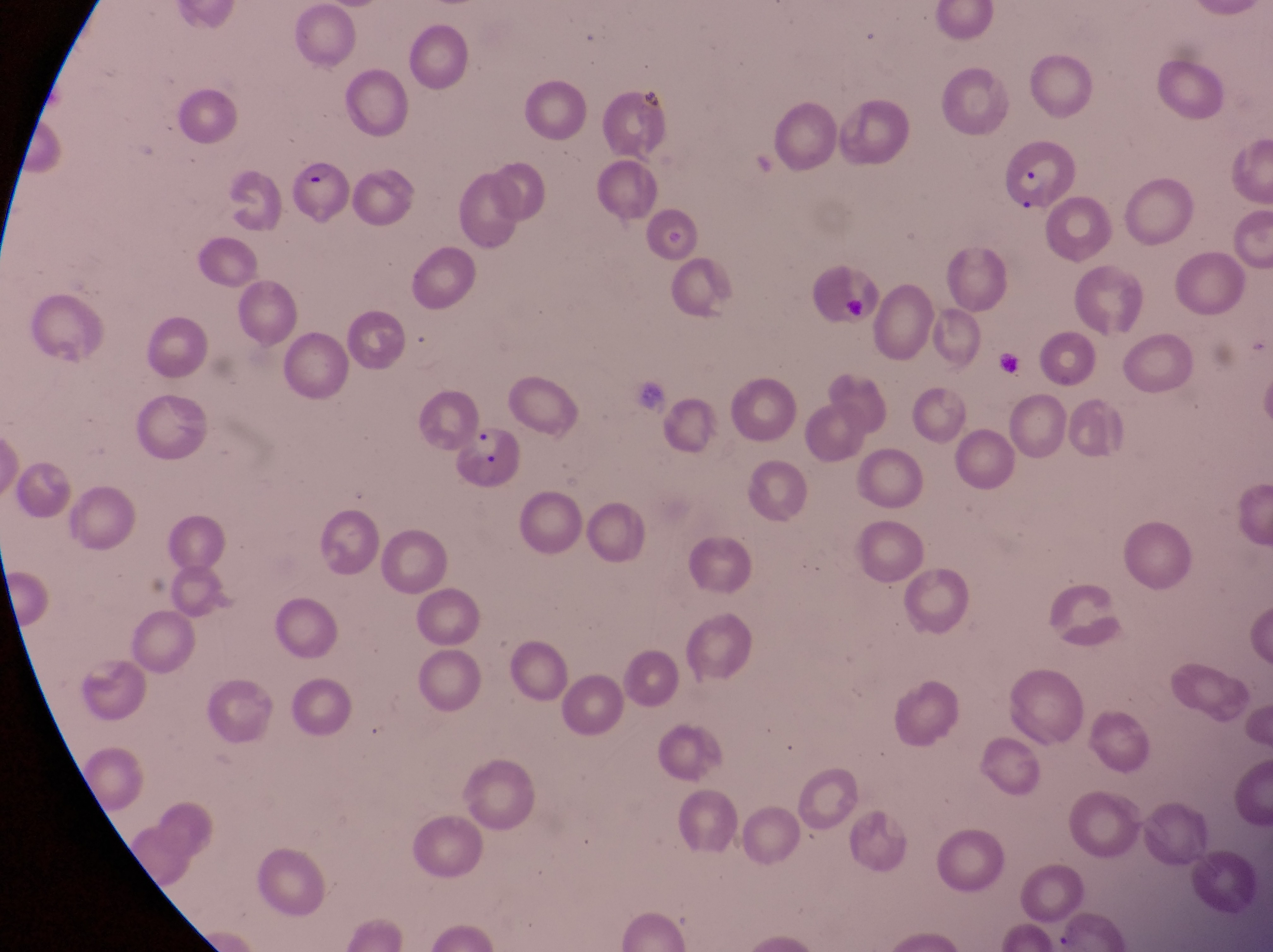

Approximate bounding boxes as {left, top, right, bottom} in pixels. Parasitised red blood cell locations: {996, 137, 1078, 207}, {292, 157, 349, 224}, {454, 424, 524, 492}. Artifact (platelet-like body, stain precipitate, or debris) locations: {843, 290, 875, 327}. Magnification of 1000x. Thin blood smear. Image is 1273×952 pixels. Sample from Uganda. Single field of view. Captured by a smartphone held over the eyepiece of an Olympus CX-23 microscope.